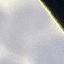

result = negative for malaria parasites
stain = Giemsa
image type = cell patch, automatically extracted from a larger field of view and resized to 64 × 64 pixels
preparation = thin blood smear
capture = smartphone through the microscope eyepiece